Assess for malaria.
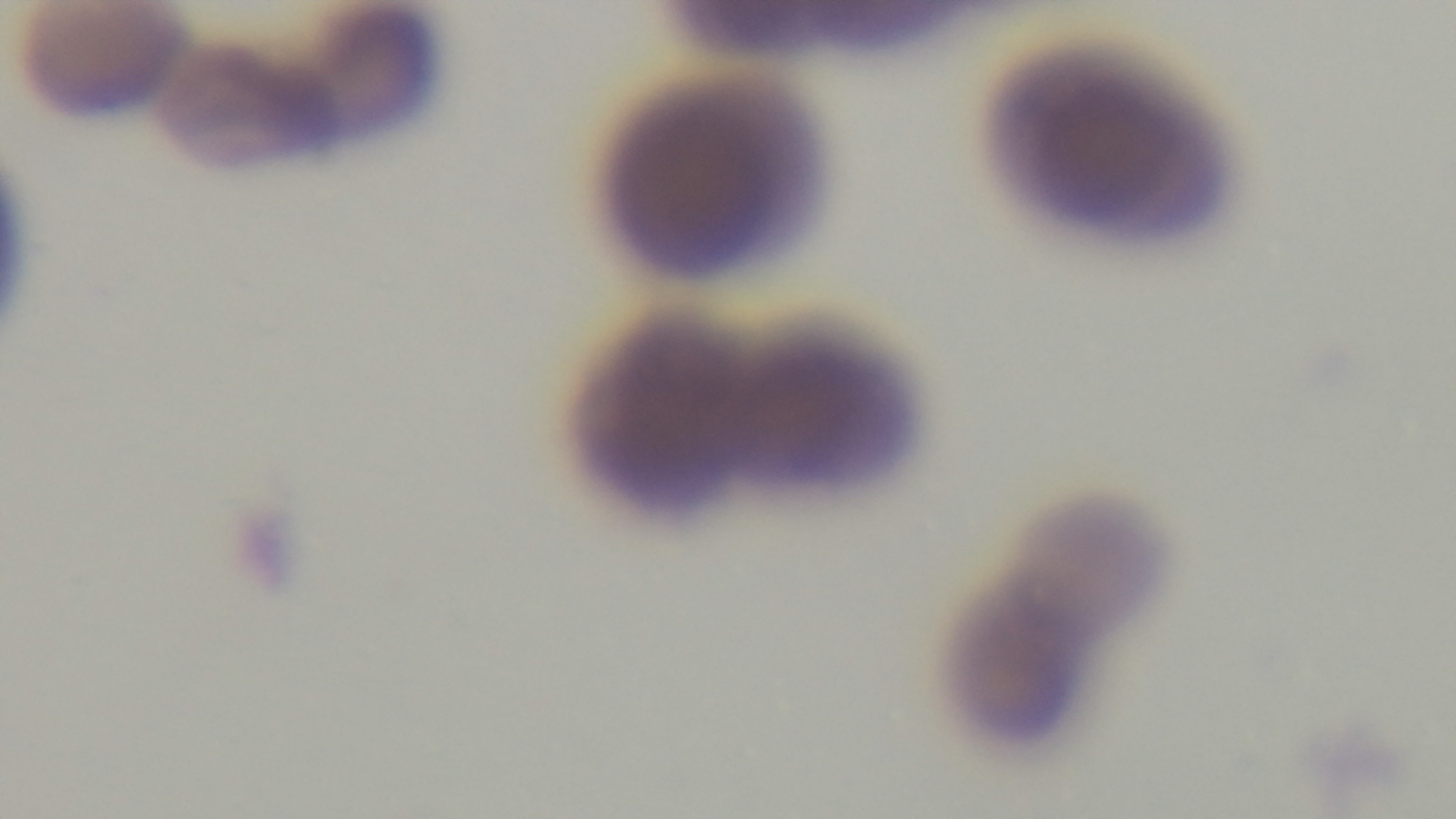
It is infected.

modality: light microscopy
objective: 100x oil immersion
capture: mounted 4K digital camera
field_of_view: one from the slide
preparation: thin blood film
stain: Giemsa